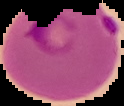
image size = 124×106 pixels
preparation = thin blood film
malaria status = parasitized
image type = segmented cell region on a black background